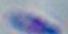
magnification = 1000x
modality = micrograph
identification = Toxoplasma gondii